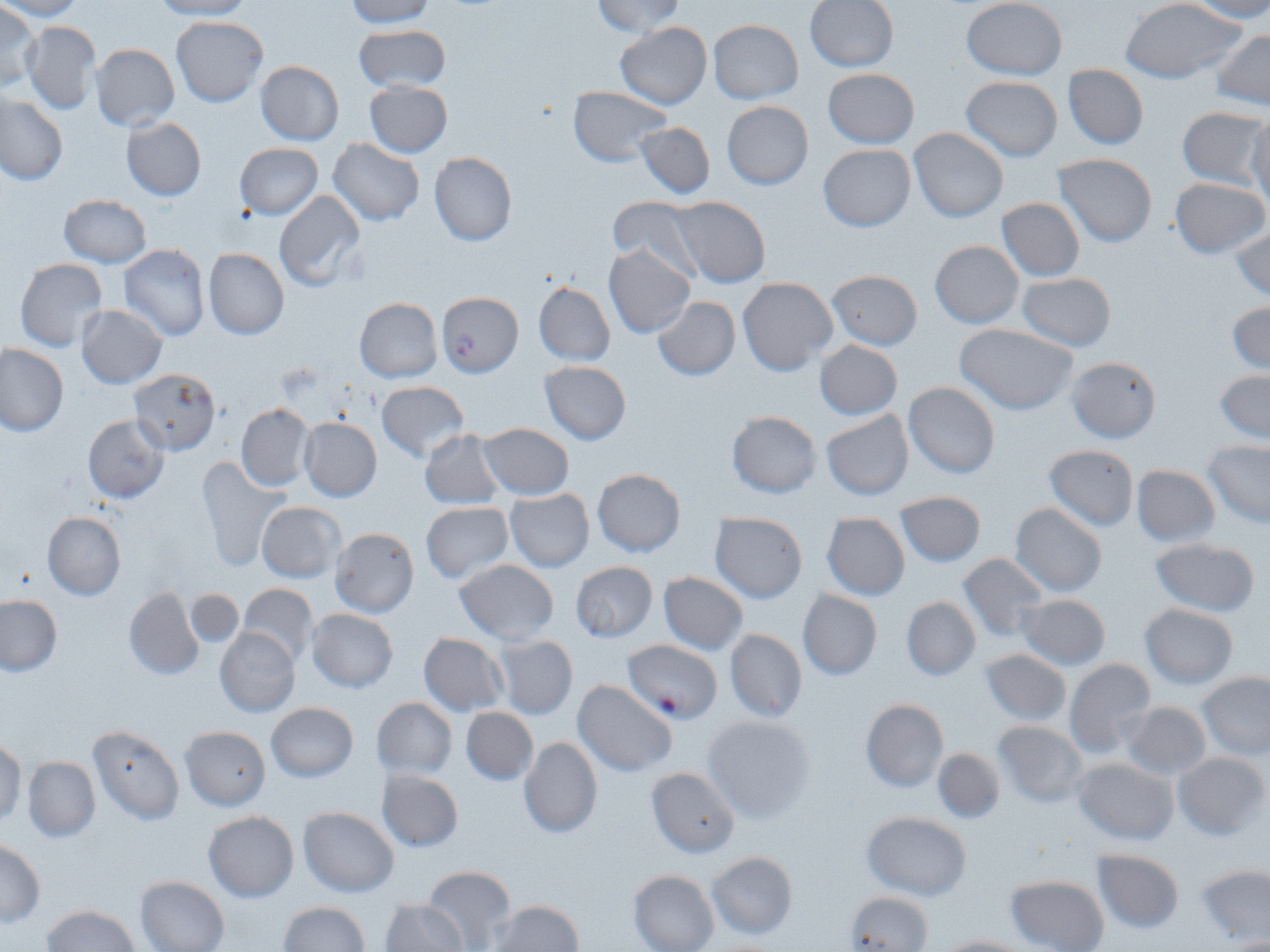

slide_level_diagnosis: Plasmodium falciparum
field_of_view: single
stain: May-Grünwald-Giemsa
uninfected_red_blood_cell_locations: 'approximate bounding boxes as [x1, y1, x2, y2] in pixels: [0, 0, 84, 20], [149, 0, 251, 20], [591, 0, 685, 37], [804, 0, 899, 72], [962, 0, 1067, 80], [1119, 0, 1245, 85], [343, 1, 437, 27], [1187, 1, 1270, 21], [0, 2, 41, 91], [171, 15, 268, 106], [708, 19, 804, 103], [23, 20, 101, 114], [615, 22, 712, 108], [354, 24, 451, 91], [1212, 28, 1270, 109], [90, 44, 179, 130], [254, 61, 343, 145], [1062, 63, 1149, 150], [822, 69, 919, 149], [960, 76, 1063, 161], [364, 82, 453, 158], [567, 87, 671, 166], [1, 93, 67, 185], [721, 101, 813, 190], [1178, 107, 1270, 190], [1248, 115, 1270, 211], [121, 117, 207, 200], [635, 121, 716, 198], [909, 128, 1007, 222], [329, 139, 424, 225], [234, 142, 323, 219], [818, 143, 916, 231], [429, 151, 518, 246], [1054, 152, 1157, 247], [1169, 178, 1267, 258], [274, 190, 366, 293], [60, 194, 150, 267], [668, 196, 771, 288], [608, 197, 703, 278], [995, 198, 1086, 281], [1230, 225, 1270, 301], [929, 240, 1024, 328], [119, 244, 209, 341], [603, 245, 696, 338], [202, 247, 289, 339], [14, 259, 107, 351], [826, 269, 922, 351], [1015, 272, 1118, 351], [738, 276, 839, 377], [533, 281, 615, 365], [652, 296, 740, 380], [354, 298, 443, 383], [1228, 301, 1270, 374], [75, 304, 168, 389], [955, 324, 1077, 416], [815, 340, 902, 420], [1, 343, 68, 436], [1067, 356, 1161, 443], [540, 361, 632, 443], [127, 367, 222, 454], [1214, 371, 1270, 443], [377, 380, 469, 462], [903, 381, 1001, 479], [236, 403, 314, 491], [820, 408, 914, 501], [726, 410, 822, 498], [82, 415, 169, 503], [298, 418, 382, 502], [477, 422, 574, 499], [419, 430, 506, 511], [1203, 441, 1270, 528], [1044, 444, 1139, 531], [197, 456, 290, 569], [1131, 465, 1222, 546], [592, 468, 686, 557], [505, 488, 595, 572], [894, 489, 986, 567], [256, 501, 344, 581], [419, 501, 514, 583], [1010, 503, 1106, 597], [41, 510, 126, 600], [710, 514, 808, 603], [822, 514, 909, 600], [329, 527, 419, 617], [1148, 538, 1262, 617], [957, 551, 1049, 641], [453, 560, 559, 641], [569, 561, 658, 642], [658, 572, 747, 656], [236, 583, 319, 669], [123, 588, 204, 679], [797, 589, 882, 679], [183, 590, 246, 649], [1016, 593, 1112, 670], [1, 595, 61, 675], [901, 596, 981, 680], [1139, 603, 1238, 689], [306, 608, 398, 693], [214, 628, 300, 717], [725, 628, 807, 722], [418, 633, 509, 716], [490, 634, 578, 720], [979, 649, 1072, 726], [1064, 659, 1157, 759], [1197, 672, 1270, 760], [573, 680, 677, 776], [371, 697, 457, 779], [860, 698, 949, 792], [266, 702, 359, 782], [1120, 702, 1212, 780], [460, 707, 537, 786], [702, 713, 816, 822], [993, 721, 1090, 807], [88, 724, 185, 825], [179, 725, 271, 810], [518, 736, 603, 838], [1, 738, 25, 827], [932, 748, 1006, 824], [1173, 750, 1267, 839], [22, 755, 101, 842], [1073, 757, 1179, 846], [646, 767, 741, 857], [377, 768, 463, 851], [297, 807, 400, 897], [203, 811, 299, 901], [861, 812, 973, 899], [0, 839, 44, 926], [1092, 847, 1185, 934], [706, 850, 798, 940], [1194, 864, 1269, 945], [422, 865, 516, 952], [629, 870, 720, 952], [1004, 874, 1110, 952], [136, 875, 230, 952], [846, 891, 932, 952], [379, 898, 468, 951], [490, 899, 584, 951], [278, 901, 368, 951], [43, 904, 139, 951], [932, 935, 1031, 952]'
image_size: 1270×952 pixels
plasmodium_falciparum_infected_red_blood_cell_locations: 'approximate bounding boxes as [x1, y1, x2, y2] in pixels: [436, 291, 523, 376], [622, 640, 723, 721]'
modality: light microscopy
preparation: thin blood film
magnification: 1000x